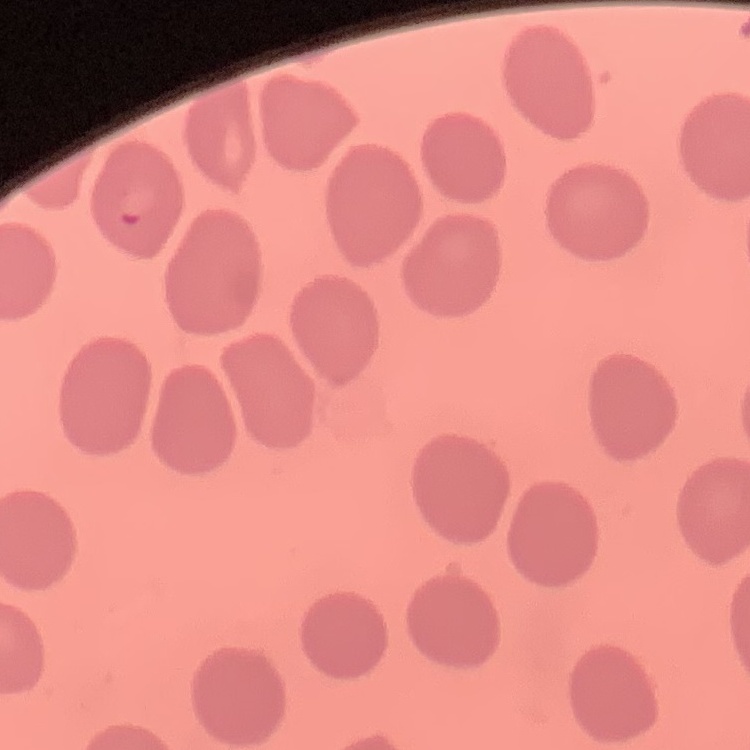
red blood cell morphology = no rouleaux formation
preparation = thin blood film
stain = Field's or Giemsa
image type = one tile cut from a larger photomicrograph